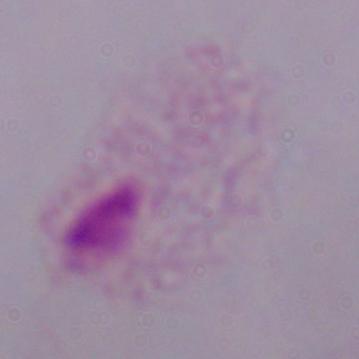
Micrograph. Captured at 1000x magnification. A trichomonad is seen.